Assess this cell for malaria.
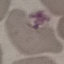

Uninfected.

{
  "preparation": "thin blood smear",
  "capture": "smartphone camera at the microscope eyepiece",
  "image_type": "cell patch, automatically extracted from a larger field of view and resized to 64 × 64 pixels",
  "stain": "Giemsa"
}